Identify the preparation type.
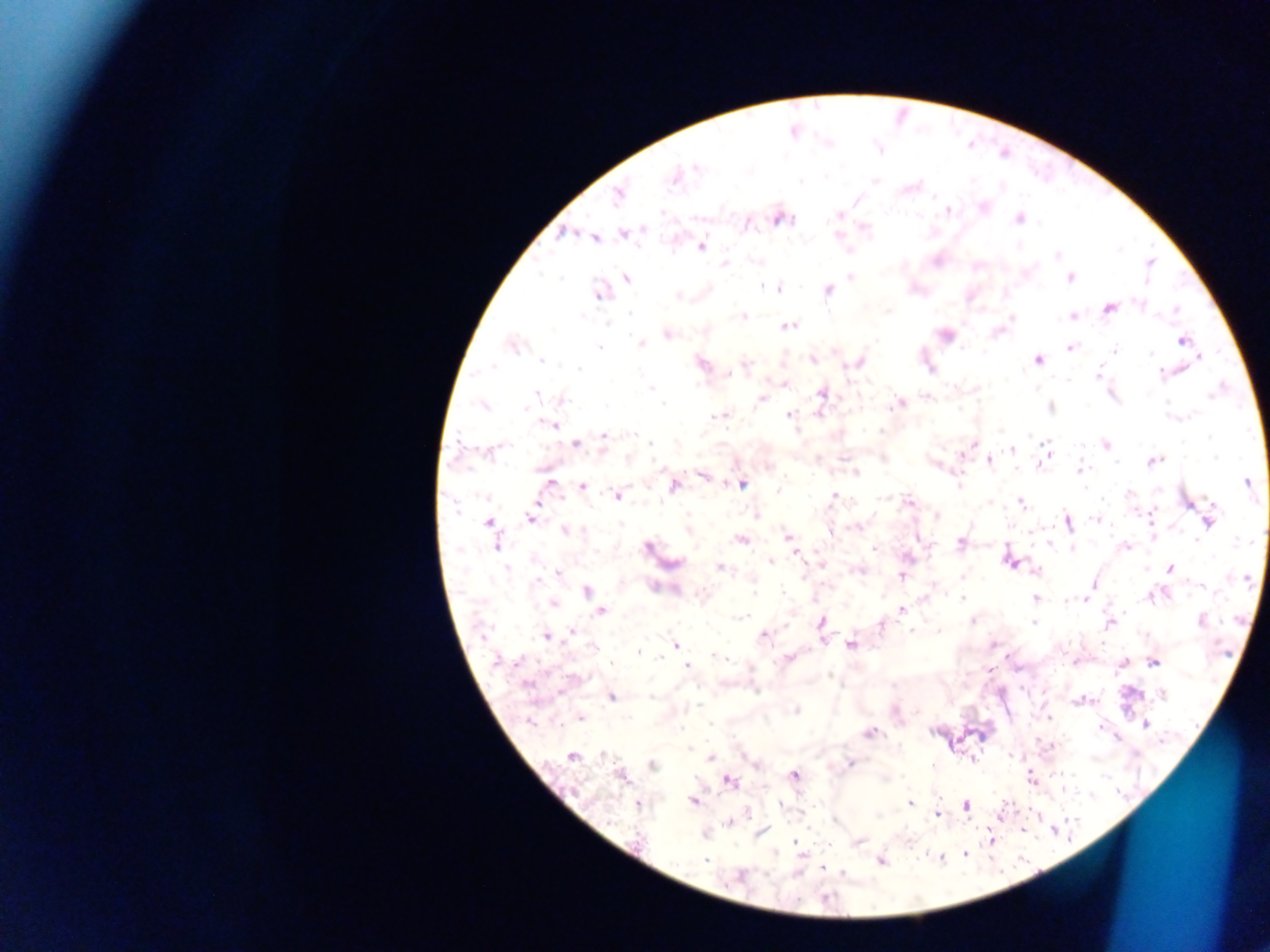
Thick blood film.

Approximate centers as [x, y] in pixels. Plasmodium parasite locations: [697, 167], [674, 176], [800, 181], [618, 196], [949, 211], [839, 215], [782, 218], [1018, 219], [562, 233], [624, 234], [594, 238], [701, 246], [1057, 256], [756, 260], [1150, 263], [725, 264], [850, 277], [627, 278], [1070, 278], [762, 286], [779, 289], [828, 290], [600, 292], [677, 296], [1139, 303], [1109, 308], [1176, 309], [889, 310], [743, 316], [1073, 317], [1012, 318], [789, 326], [667, 334], [1182, 341], [641, 344], [512, 345], [1070, 347], [600, 348], [1115, 350], [1150, 353], [1199, 356], [812, 359], [1038, 360], [542, 361], [858, 362], [702, 363], [746, 364], [492, 367], [579, 369], [1097, 373], [729, 374], [1161, 374], [785, 383], [651, 388], [822, 393], [536, 394], [762, 398], [563, 400], [663, 404], [898, 404], [484, 405], [1050, 408], [820, 412], [789, 415], [717, 416], [549, 423], [881, 430], [604, 436], [649, 443], [576, 444], [972, 444], [1105, 445], [1011, 450], [990, 460], [1154, 461], [1040, 464], [1079, 469], [856, 472], [703, 475], [549, 483], [1247, 483], [741, 484], [959, 485], [583, 486], [673, 486], [1129, 494], [618, 495], [834, 496], [908, 501], [1021, 503], [756, 515], [937, 516], [531, 518], [1095, 519], [1067, 522], [1209, 522], [488, 523], [688, 529], [565, 530], [831, 531], [788, 537], [740, 540], [1195, 540], [961, 543], [496, 544], [1050, 544], [648, 547], [1126, 547], [874, 548], [1072, 548], [907, 557], [1009, 560], [771, 562], [674, 563], [506, 568], [720, 568], [1171, 569], [858, 570], [1036, 571], [559, 572], [901, 576], [538, 581], [1093, 584], [655, 587], [1201, 587], [587, 590], [1152, 596], [962, 598], [1035, 598], [1084, 600], [1070, 601], [553, 603], [901, 610], [601, 611], [740, 617], [1202, 620], [972, 621], [1034, 622], [1110, 622], [821, 623], [882, 625], [572, 631], [763, 635], [545, 636], [676, 644], [851, 644], [593, 647], [639, 652], [718, 658], [788, 658], [498, 661], [1154, 663], [687, 666], [989, 669], [1163, 695], [611, 697], [796, 711], [580, 718], [529, 721], [1146, 724], [869, 732], [603, 754], [573, 756], [710, 758], [851, 762], [652, 765], [794, 776], [1031, 777], [730, 782], [693, 801], [910, 802], [637, 805], [966, 806], [937, 814], [729, 822], [991, 839], [858, 842], [966, 852], [705, 859], [881, 861]. One field of view. Collected in Ghana. Image is 1270×952 pixels. Photographed through a microscope with a mobile-phone camera.